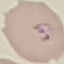
Summary:
  - Result: malaria parasites identified
  - Stain: Giemsa
  - Preparation: thin blood smear
  - Image type: automatically extracted cell patch, resized to 64 × 64 pixels
  - Capture: smartphone through the microscope eyepiece